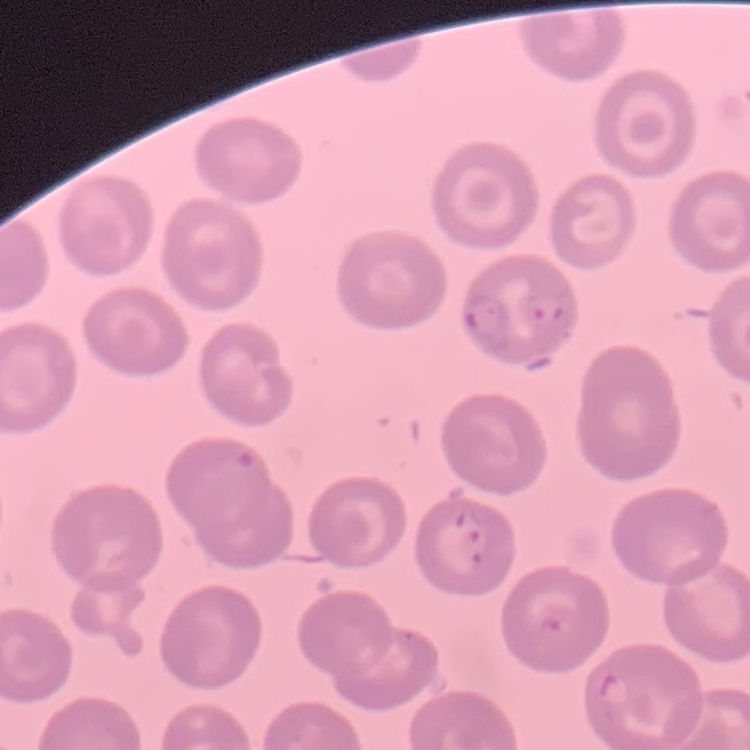

Summary:
  - Erythrocyte morphology: no rouleaux formation
  - Stain: Field's or Giemsa
  - Preparation: thin peripheral smear
  - Image type: square crop of a larger photomicrograph